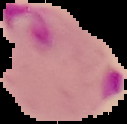
From a thin blood film. Segmented cell region on a black background. Image is 127×124 pixels. Result: malaria parasites identified.